Identify the blood parasite species.
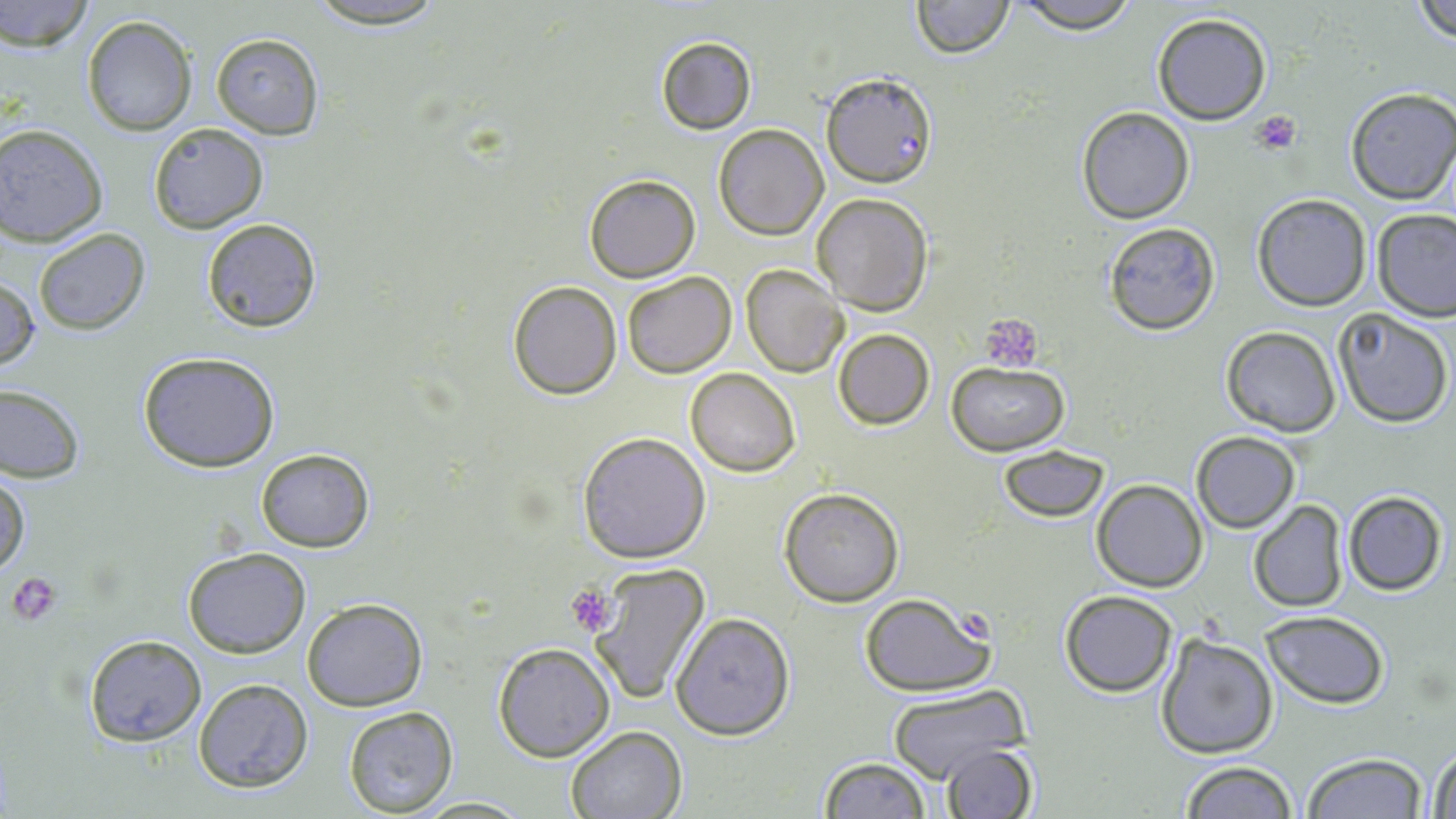
Plasmodium falciparum.

Approximate bounding boxes as (x1, y1, x2, y2) in pixels. Platelet locations: (1253, 109, 1303, 153), (979, 316, 1047, 370), (7, 571, 63, 626), (565, 585, 618, 637), (959, 613, 995, 648). Plasmodium falciparum-infected red blood cell locations: (819, 71, 936, 188). Uninfected red blood cell locations: (1, 0, 95, 49), (300, 0, 453, 29), (910, 0, 1014, 57), (1010, 0, 1142, 33), (1410, 0, 1456, 44), (1151, 13, 1273, 124), (80, 15, 198, 136), (210, 33, 324, 139), (656, 35, 757, 134), (1344, 89, 1456, 205), (1076, 106, 1195, 224), (148, 122, 267, 233), (1, 124, 111, 246), (713, 124, 828, 240), (585, 173, 700, 281), (810, 193, 934, 313), (1252, 194, 1370, 311), (1371, 209, 1456, 322), (201, 217, 323, 334), (1101, 221, 1220, 336), (34, 228, 150, 336), (741, 265, 849, 379), (621, 273, 737, 379), (0, 276, 39, 374), (508, 281, 622, 400), (1333, 309, 1453, 429), (1221, 326, 1342, 438), (832, 328, 934, 430), (136, 351, 282, 473), (947, 362, 1067, 454), (686, 368, 799, 476), (0, 383, 84, 482), (576, 431, 710, 562), (1190, 431, 1301, 532), (998, 445, 1109, 522), (255, 448, 374, 552), (0, 470, 29, 581), (1091, 478, 1208, 592), (779, 488, 904, 606), (1342, 491, 1447, 595), (1248, 500, 1350, 614), (182, 546, 312, 658), (585, 563, 711, 706), (1059, 590, 1177, 696), (857, 595, 994, 699), (301, 600, 428, 711), (1262, 611, 1391, 708), (671, 612, 795, 740), (1155, 630, 1280, 759), (84, 636, 205, 746), (493, 642, 616, 762), (193, 678, 314, 793), (888, 686, 1026, 782), (344, 706, 457, 817), (565, 725, 688, 819), (939, 742, 1038, 819), (1426, 742, 1456, 819), (1302, 752, 1428, 819), (817, 756, 933, 819), (1180, 761, 1299, 818), (418, 795, 529, 816). Light microscopy. Single field of view. May-Grünwald-Giemsa stain. Image is 1456×819 pixels. Thin blood film. Captured at 1000x magnification.